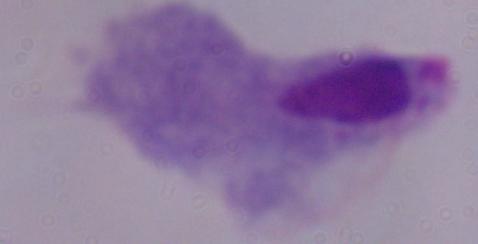
Summary:
  - Magnification: 1000x
  - Identification: trichomonad
  - Modality: micrograph